Locate every blood parasite and identify its species.
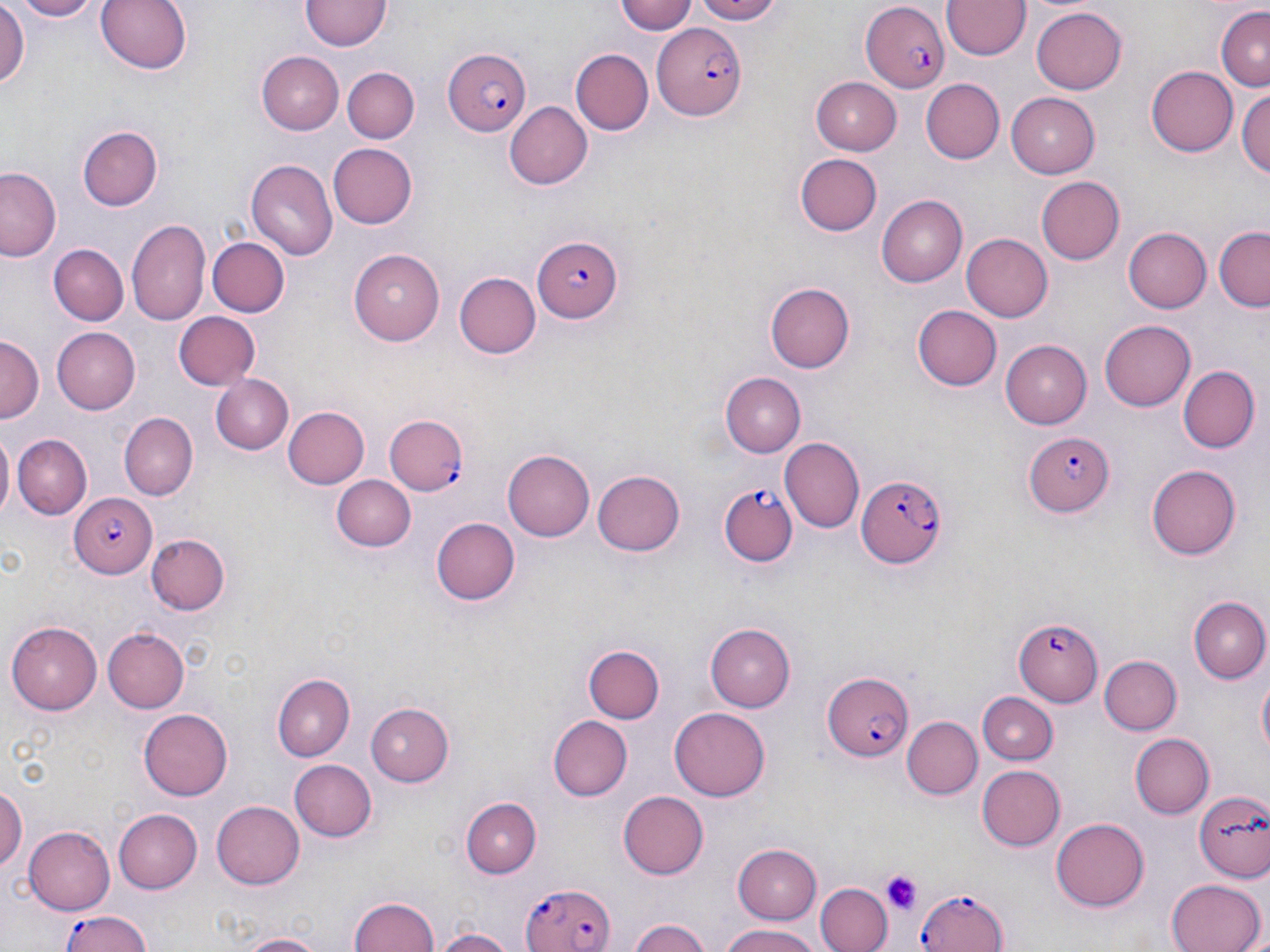

Approximate bounding boxes as named x1/y1/x2/y2 corners in pixels.
Plasmodium falciparum-infected red blood cells: (x1=860, y1=5, x2=949, y2=92), (x1=654, y1=24, x2=744, y2=119), (x1=441, y1=47, x2=531, y2=134), (x1=531, y1=237, x2=624, y2=321), (x1=384, y1=413, x2=466, y2=493), (x1=1024, y1=430, x2=1116, y2=517), (x1=854, y1=473, x2=945, y2=568), (x1=720, y1=484, x2=798, y2=566), (x1=68, y1=493, x2=156, y2=576), (x1=1012, y1=619, x2=1102, y2=707), (x1=819, y1=671, x2=914, y2=762), (x1=523, y1=882, x2=613, y2=952), (x1=911, y1=887, x2=1010, y2=952), (x1=56, y1=913, x2=152, y2=952).
No Plasmodium ovale, Plasmodium malariae, Plasmodium vivax, Babesia divergens, or Trypanosoma brucei observed.

slide-level diagnosis = Plasmodium falciparum
field of view = single
preparation = thin blood film
modality = light microscopy
stain = May-Grünwald-Giemsa
platelet locations = approximate bounding boxes as named x1/y1/x2/y2 corners in pixels: (x1=879, y1=872, x2=922, y2=914)
image size = 1270×952 pixels
uninfected red blood cell locations = approximate bounding boxes as named x1/y1/x2/y2 corners in pixels: (x1=8, y1=0, x2=104, y2=21), (x1=96, y1=0, x2=193, y2=75), (x1=615, y1=0, x2=699, y2=34), (x1=689, y1=0, x2=788, y2=24), (x1=300, y1=1, x2=390, y2=53), (x1=942, y1=1, x2=1029, y2=61), (x1=0, y1=3, x2=29, y2=91), (x1=1214, y1=6, x2=1270, y2=90), (x1=1029, y1=7, x2=1129, y2=95), (x1=570, y1=48, x2=653, y2=134), (x1=257, y1=52, x2=343, y2=134), (x1=342, y1=67, x2=418, y2=143), (x1=1146, y1=67, x2=1236, y2=155), (x1=812, y1=76, x2=904, y2=153), (x1=921, y1=79, x2=1005, y2=164), (x1=1238, y1=89, x2=1270, y2=181), (x1=1006, y1=92, x2=1100, y2=177), (x1=505, y1=101, x2=590, y2=188), (x1=76, y1=126, x2=163, y2=211), (x1=327, y1=142, x2=417, y2=229), (x1=796, y1=155, x2=881, y2=236), (x1=246, y1=159, x2=338, y2=260), (x1=0, y1=166, x2=63, y2=264), (x1=1036, y1=176, x2=1125, y2=264), (x1=878, y1=195, x2=968, y2=287), (x1=127, y1=219, x2=210, y2=324), (x1=1122, y1=227, x2=1211, y2=314), (x1=1214, y1=227, x2=1270, y2=308), (x1=961, y1=233, x2=1052, y2=322), (x1=209, y1=235, x2=288, y2=315), (x1=47, y1=244, x2=129, y2=326), (x1=352, y1=248, x2=445, y2=344), (x1=454, y1=271, x2=542, y2=357), (x1=767, y1=283, x2=855, y2=372), (x1=913, y1=306, x2=1001, y2=390), (x1=172, y1=311, x2=260, y2=391), (x1=1101, y1=318, x2=1196, y2=408), (x1=52, y1=326, x2=140, y2=414), (x1=0, y1=336, x2=42, y2=426), (x1=1000, y1=339, x2=1093, y2=428), (x1=1177, y1=366, x2=1257, y2=453), (x1=721, y1=374, x2=804, y2=456), (x1=209, y1=375, x2=297, y2=454), (x1=282, y1=406, x2=367, y2=489), (x1=119, y1=411, x2=197, y2=498), (x1=1, y1=431, x2=15, y2=522), (x1=13, y1=433, x2=91, y2=518), (x1=779, y1=439, x2=864, y2=533), (x1=502, y1=449, x2=593, y2=542), (x1=1147, y1=466, x2=1242, y2=559), (x1=593, y1=469, x2=686, y2=556), (x1=332, y1=474, x2=415, y2=552), (x1=433, y1=515, x2=523, y2=605), (x1=146, y1=535, x2=229, y2=616), (x1=1188, y1=596, x2=1270, y2=684), (x1=7, y1=620, x2=103, y2=714), (x1=707, y1=624, x2=795, y2=711), (x1=103, y1=628, x2=190, y2=712), (x1=584, y1=645, x2=664, y2=724), (x1=1099, y1=653, x2=1181, y2=734), (x1=273, y1=672, x2=354, y2=762), (x1=1256, y1=672, x2=1270, y2=761), (x1=978, y1=691, x2=1056, y2=766), (x1=365, y1=699, x2=457, y2=787), (x1=138, y1=708, x2=232, y2=800), (x1=669, y1=708, x2=771, y2=801), (x1=549, y1=716, x2=632, y2=801), (x1=902, y1=717, x2=982, y2=801), (x1=1129, y1=733, x2=1213, y2=819), (x1=287, y1=758, x2=377, y2=843), (x1=978, y1=764, x2=1064, y2=850), (x1=0, y1=785, x2=25, y2=876), (x1=617, y1=791, x2=709, y2=880), (x1=1195, y1=791, x2=1270, y2=883), (x1=462, y1=796, x2=541, y2=876), (x1=213, y1=800, x2=305, y2=890), (x1=109, y1=807, x2=201, y2=895), (x1=1052, y1=818, x2=1150, y2=910), (x1=24, y1=826, x2=115, y2=915), (x1=733, y1=844, x2=824, y2=924), (x1=1165, y1=879, x2=1263, y2=952), (x1=817, y1=883, x2=891, y2=952), (x1=350, y1=895, x2=440, y2=952), (x1=629, y1=918, x2=713, y2=952), (x1=721, y1=925, x2=823, y2=952), (x1=432, y1=927, x2=517, y2=952), (x1=235, y1=932, x2=327, y2=952)
magnification = 1000x